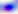

identification: Toxoplasma gondii
modality: micrograph
magnification: 400x